Assess this cell for malaria.
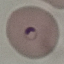

Parasitized.

Automatically extracted cell patch, resized to 64 × 64 pixels. Thin blood smear. Giemsa stain. Photographed with a smartphone camera at the microscope eyepiece.